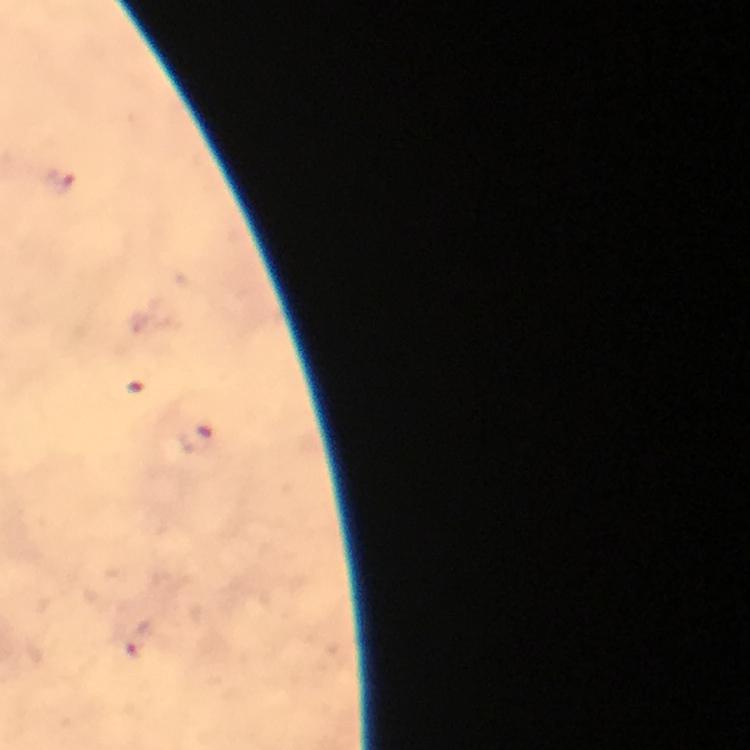
Approximate centers as [x, y] in pixels. Malaria parasite locations: [59, 182], [132, 388], [195, 437], [141, 640]. Smartphone photograph taken through a microscope. Image is 750×750 pixels. Giemsa stain. From a diagnostic examination for malaria. Thick blood smear. 100x magnification. A crop from one field of view. Immersion oil was used.